Name the cell type shown.
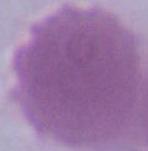

This is an erythrocyte.

{
  "magnification": "1000x",
  "modality": "photomicrograph"
}